Name the blood parasite species.
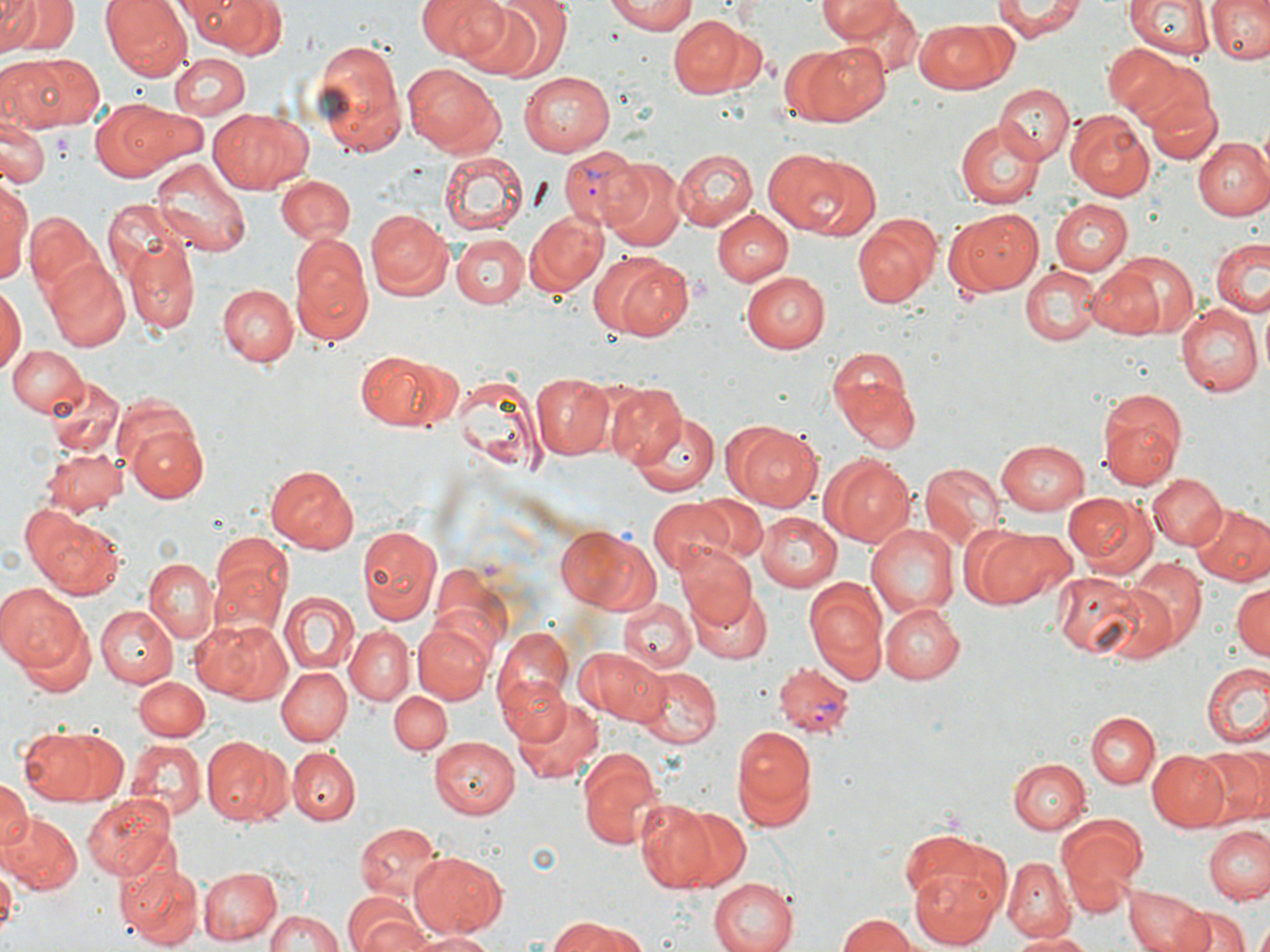

Plasmodium vivax.

modality = light microscopy
stain = May-Grünwald-Giemsa
platelet locations = approximate bounding boxes as [x1, y1, x2, y2] in pixels: [50, 133, 73, 162], [690, 273, 710, 299]
preparation = thin blood smear
magnification = 1000x
uninfected red blood cell locations = approximate bounding boxes as [x1, y1, x2, y2] in pixels: [1, 0, 37, 48], [1, 0, 73, 58], [102, 0, 192, 81], [191, 0, 288, 58], [416, 0, 508, 61], [492, 0, 573, 77], [607, 0, 698, 34], [817, 0, 904, 42], [994, 0, 1086, 41], [1125, 0, 1212, 61], [1206, 0, 1270, 64], [453, 2, 548, 80], [820, 3, 920, 74], [667, 13, 759, 99], [914, 20, 1009, 93], [311, 37, 408, 160], [791, 40, 891, 126], [1102, 42, 1185, 118], [8, 52, 105, 132], [1118, 52, 1215, 138], [171, 53, 250, 118], [403, 61, 504, 154], [517, 71, 615, 157], [995, 85, 1072, 164], [1151, 94, 1222, 166], [90, 100, 180, 180], [118, 105, 208, 170], [210, 106, 312, 194], [1069, 114, 1155, 201], [1, 119, 47, 192], [954, 120, 1042, 208], [1193, 137, 1268, 221], [762, 147, 864, 237], [672, 149, 758, 230], [436, 151, 529, 237], [805, 157, 880, 241], [151, 158, 253, 255], [602, 158, 686, 251], [276, 174, 354, 245], [0, 175, 31, 289], [1049, 198, 1131, 276], [720, 206, 810, 343], [364, 208, 451, 296], [712, 208, 793, 286], [947, 208, 1042, 296], [525, 209, 606, 294], [25, 210, 106, 301], [852, 218, 940, 307], [288, 230, 373, 348], [451, 233, 528, 309], [1211, 235, 1269, 318], [127, 242, 200, 334], [1107, 249, 1201, 338], [596, 251, 691, 340], [44, 258, 131, 352], [1085, 263, 1166, 340], [1021, 268, 1100, 346], [740, 270, 829, 352], [219, 285, 298, 365], [0, 286, 23, 377], [1175, 301, 1262, 396], [9, 343, 88, 419], [358, 352, 448, 431], [831, 355, 921, 451], [454, 370, 541, 476], [533, 373, 614, 459], [45, 375, 125, 458], [604, 383, 686, 467], [1097, 388, 1186, 487], [629, 409, 721, 495], [122, 418, 209, 502], [728, 420, 822, 512], [995, 438, 1091, 515], [43, 448, 128, 516], [822, 455, 913, 546], [920, 462, 1004, 547], [263, 465, 359, 552], [1148, 474, 1226, 550], [1063, 491, 1153, 576], [685, 493, 766, 564], [648, 498, 735, 577], [1192, 503, 1269, 587], [24, 510, 125, 599], [754, 511, 843, 591], [866, 523, 959, 620], [959, 523, 1070, 610], [557, 524, 657, 614], [356, 525, 443, 627], [207, 532, 292, 631], [676, 544, 759, 631], [142, 556, 219, 642], [1127, 557, 1207, 644], [1053, 572, 1143, 656], [803, 576, 887, 685], [1230, 580, 1269, 662], [0, 583, 86, 674], [690, 583, 776, 664], [278, 590, 357, 675], [618, 598, 695, 675], [879, 601, 963, 683], [94, 605, 178, 686], [13, 612, 97, 700], [191, 617, 296, 702], [411, 622, 493, 706], [344, 625, 416, 704], [491, 628, 575, 724], [578, 647, 667, 727], [1201, 661, 1270, 750], [634, 664, 722, 748], [276, 667, 350, 745], [133, 676, 208, 741], [499, 677, 573, 747], [388, 691, 453, 755], [512, 694, 603, 783], [1087, 712, 1158, 789], [729, 724, 818, 833], [21, 727, 105, 804], [201, 737, 290, 825], [429, 737, 518, 818], [127, 739, 205, 817], [575, 746, 664, 851], [1194, 747, 1269, 828], [287, 748, 359, 823], [1146, 750, 1230, 832], [1009, 758, 1090, 833], [0, 780, 31, 853], [82, 792, 178, 881], [635, 799, 720, 893], [672, 804, 750, 891], [0, 811, 80, 896], [1056, 816, 1147, 912], [357, 821, 444, 901], [1206, 824, 1270, 904], [898, 826, 1012, 927], [408, 849, 508, 935], [1003, 856, 1073, 941], [0, 857, 17, 940], [120, 862, 203, 949], [909, 866, 1004, 946], [198, 867, 284, 944], [707, 876, 800, 952], [1124, 885, 1203, 952], [343, 895, 432, 952], [1174, 905, 1248, 952], [267, 911, 345, 952], [836, 913, 925, 952], [543, 919, 650, 952], [1251, 922, 1270, 952], [408, 930, 498, 952], [1004, 930, 1092, 951]
Plasmodium vivax-infected red blood cell locations = approximate bounding boxes as [x1, y1, x2, y2] in pixels: [559, 147, 645, 231], [772, 667, 855, 738]
field of view = single
image size = 1270×952 pixels